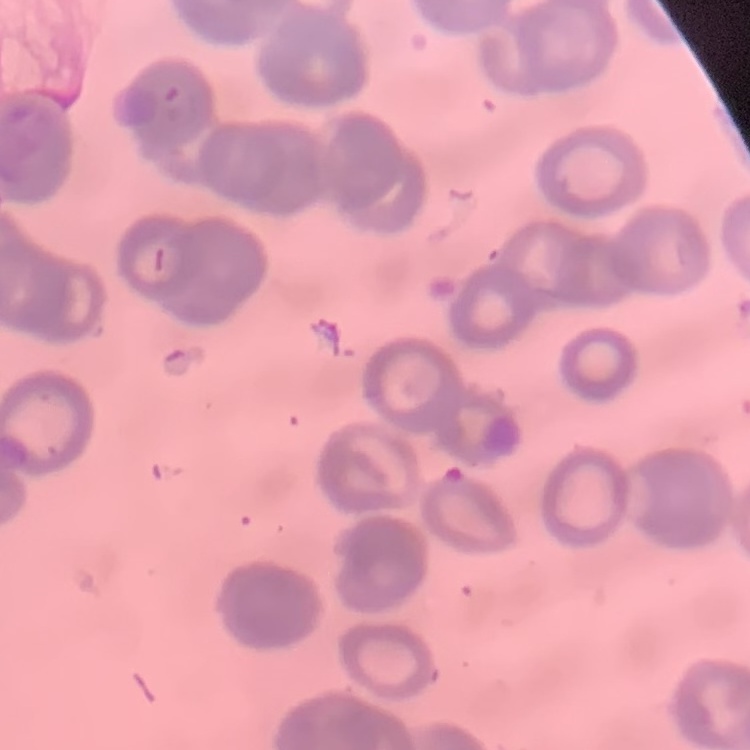
Summary:
  - Erythrocyte morphology: rouleaux formation
  - Preparation: thin peripheral smear
  - Image type: square crop of a larger photomicrograph
  - Stain: Field's or Giemsa